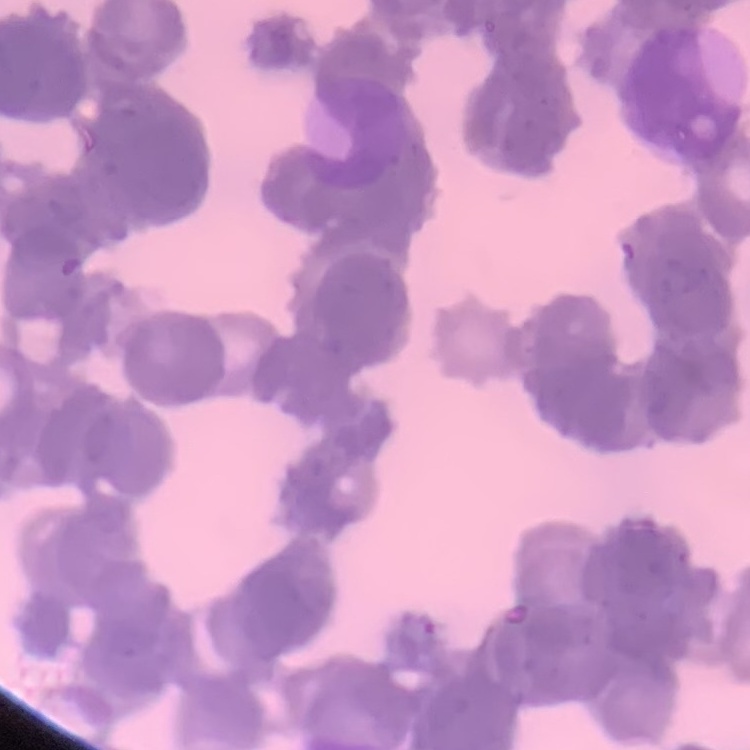 The erythrocytes exhibit rouleaux formation. Thin peripheral smear. One tile cut from a larger photomicrograph. Field's or Giemsa stain.